Report the malaria status of this cell.
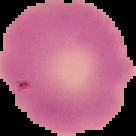
It is uninfected.

From a thin blood film. The area outside the segmented cell region is set to black. Image is 136×136 pixels.